Comment on the morphology of the erythrocytes.
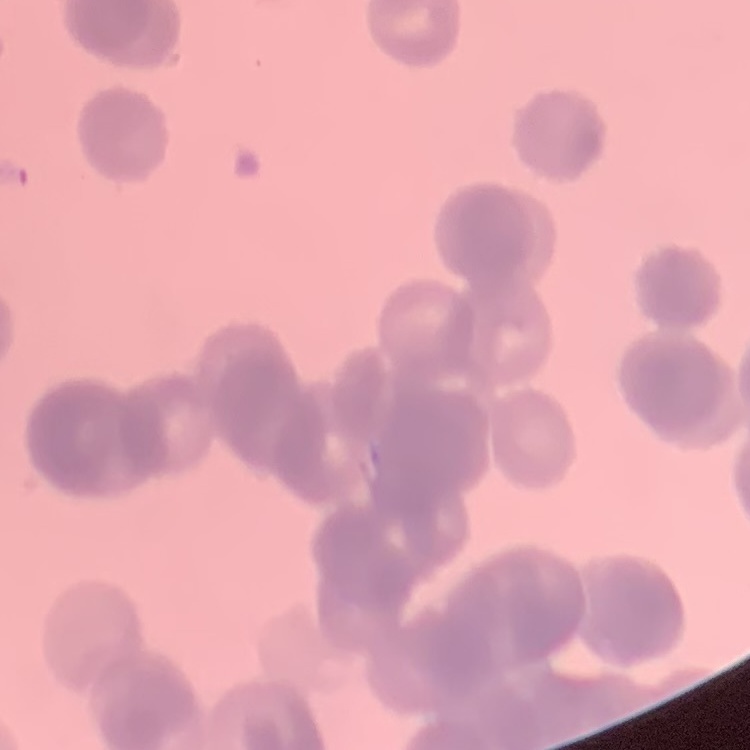
They show rouleaux formation.

Thin blood smear. One tile cut from a larger photomicrograph. Field's or Giemsa stain.